Identify the parasite.
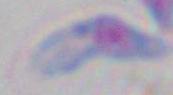
This is Toxoplasma gondii.

modality = photomicrograph
magnification = 1000x